Outline each blood parasite and name the species.
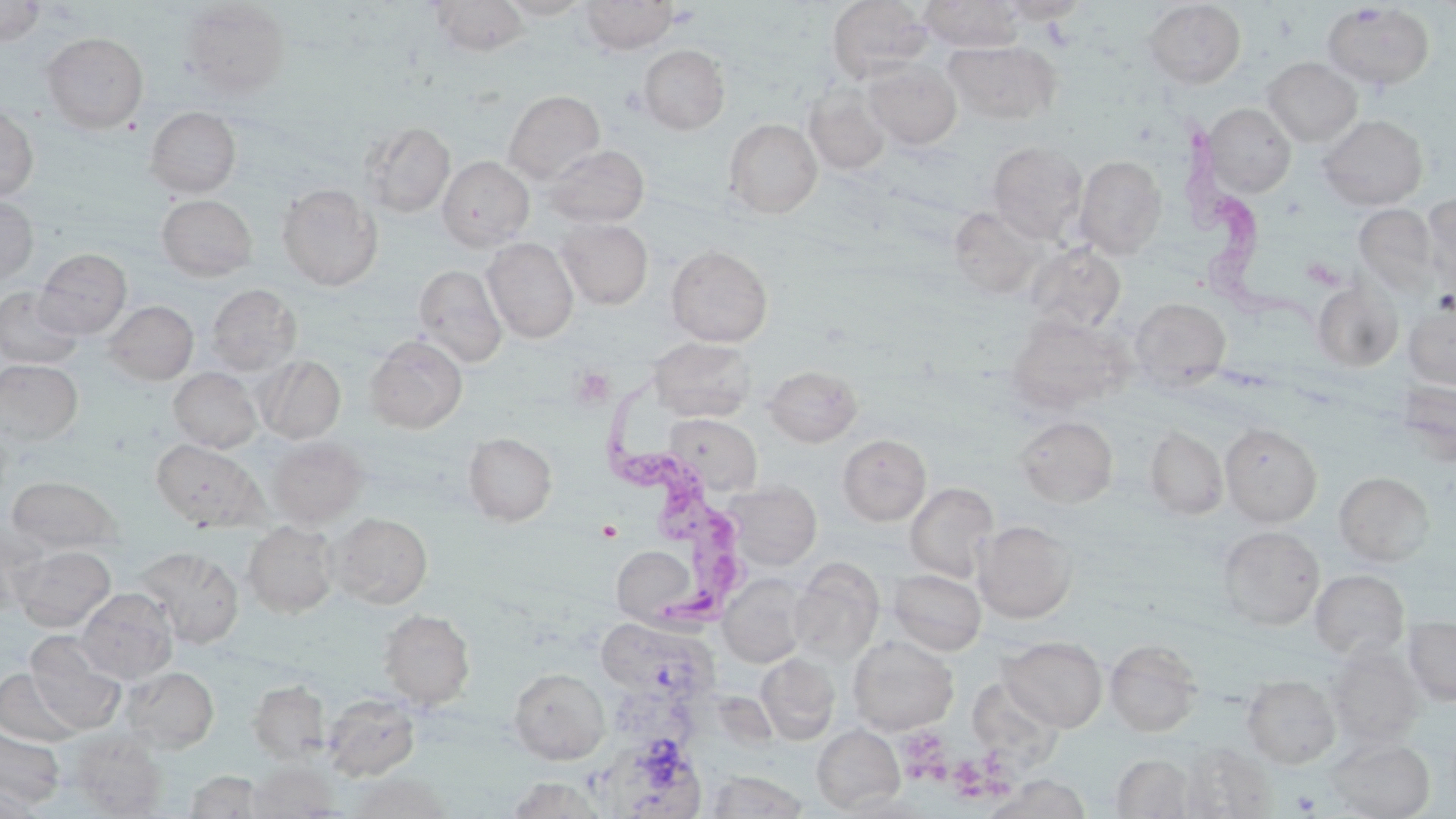
Approximate bounding boxes as (x1,y1)-(x2,y2) corner pairs in pixels.
Trypanosoma brucei: (1170,116)-(1318,336), (609,380)-(757,639).
No Plasmodium falciparum, Plasmodium ovale, Plasmodium malariae, Plasmodium vivax, or Babesia divergens observed.

Summary:
  - Platelet locations: (570,366)-(615,407), (910,733)-(957,790), (946,745)-(1018,801), (1292,791)-(1320,814)
  - Uninfected red blood cell locations: (428,0)-(530,56), (497,0)-(592,19), (580,0)-(678,53), (826,0)-(932,83), (919,0)-(1025,51), (996,0)-(1092,22), (0,1)-(44,46), (179,1)-(291,99), (1143,1)-(1246,88), (1321,2)-(1435,91), (41,32)-(148,133), (943,40)-(1062,125), (638,44)-(730,134), (1262,57)-(1363,146), (862,60)-(962,149), (803,84)-(891,174), (503,90)-(605,183), (0,102)-(39,203), (1201,103)-(1296,197), (145,106)-(241,197), (1317,113)-(1428,211), (724,118)-(822,219), (360,121)-(455,217), (988,141)-(1087,243), (543,144)-(650,228), (1074,154)-(1166,260), (437,156)-(535,250), (277,183)-(383,291), (1421,192)-(1456,296), (157,194)-(257,281), (0,196)-(38,283), (1354,204)-(1441,298), (948,206)-(1048,299), (556,218)-(653,309), (482,238)-(578,343), (1025,242)-(1126,333), (666,245)-(773,347), (34,248)-(132,338), (413,264)-(507,368), (1312,281)-(1404,372), (206,284)-(301,375), (1,285)-(83,369), (1129,297)-(1231,390), (103,300)-(198,385), (1403,301)-(1456,390), (1006,313)-(1132,413), (365,334)-(467,433), (648,336)-(757,422), (256,355)-(346,444), (0,359)-(83,447), (764,364)-(862,447), (169,367)-(262,453), (1396,380)-(1456,464), (665,413)-(763,497), (1014,415)-(1118,507), (0,421)-(13,511), (1220,423)-(1322,527), (1146,426)-(1228,519), (463,433)-(557,525), (838,434)-(931,525), (267,436)-(368,527), (151,439)-(264,530), (1335,472)-(1433,567), (6,475)-(123,554), (723,480)-(821,570), (905,482)-(999,582), (328,512)-(433,608), (0,518)-(44,617), (974,520)-(1077,623), (242,521)-(338,618), (1217,525)-(1325,630), (10,544)-(116,631), (612,545)-(698,625), (135,546)-(244,648), (789,558)-(884,664), (888,568)-(986,655), (1310,569)-(1409,661), (718,574)-(810,668), (76,587)-(178,683), (379,609)-(475,709), (1403,616)-(1456,705), (598,620)-(721,698), (25,633)-(128,734), (848,635)-(958,734), (999,636)-(1108,732), (1105,639)-(1202,736), (1328,647)-(1423,748), (756,653)-(840,745), (119,665)-(219,754), (509,667)-(609,764), (0,668)-(83,748), (1242,675)-(1340,768), (967,677)-(1063,771), (248,681)-(329,763), (323,692)-(421,781), (812,724)-(905,813), (0,725)-(65,809), (68,729)-(167,817), (1326,737)-(1436,818), (602,739)-(709,817), (1178,742)-(1277,818), (1111,754)-(1194,818), (248,762)-(338,817), (183,770)-(266,818), (705,771)-(807,818), (345,772)-(453,818), (985,774)-(1090,819), (507,777)-(606,818), (0,782)-(41,819), (839,792)-(936,818)
  - Slide-level diagnosis: Trypanosoma brucei
  - Image size: 1456×819 pixels
  - Preparation: thin blood smear
  - Field of view: one of a larger specimen
  - Stain: May-Grünwald-Giemsa
  - Magnification: 1000x
  - Modality: light microscopy